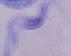

Summary:
  - Magnification: 1000x
  - Identification: trypanosome
  - Modality: photomicrograph